Assess this cell for malaria.
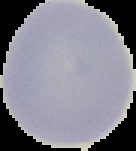

It is uninfected.

Summary:
  - Image size: 136×151 pixels
  - Image type: segmented cell region on a black background
  - Preparation: thin blood smear